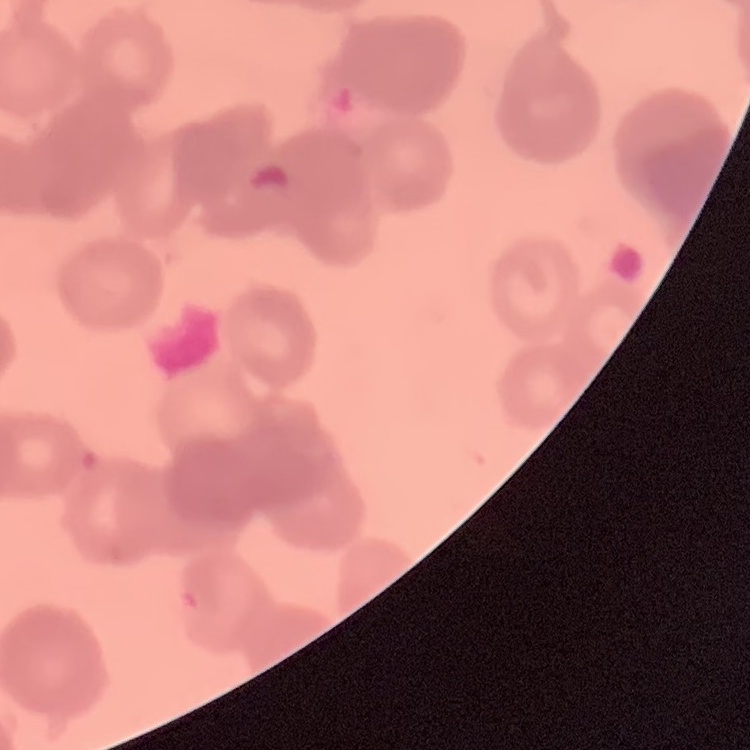

Summary:
  - Erythrocyte morphology: rouleaux formation
  - Preparation: thin peripheral smear
  - Stain: Field's or Giemsa
  - Image type: square crop of a larger photomicrograph